Point out each malaria parasite.
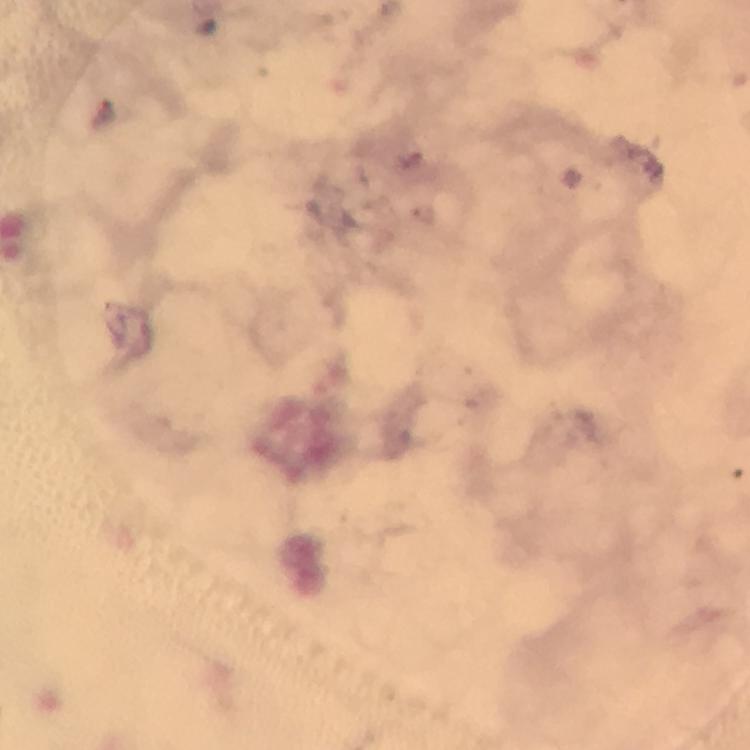

Approximate centers as (x, y) in pixels.
Malaria parasites: (107, 114).

Cropped region of a single field of view. Image is 750×750 pixels. Thick smear. From a malaria diagnostic workup. Photographed through the microscope with a smartphone camera. 100x magnification. Immersion oil was used. Giemsa stain.